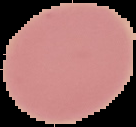

Summary:
  - Image size: 136×127 pixels
  - Preparation: thin blood film
  - Malaria status: uninfected
  - Image type: segmented cell region with the area outside set to black